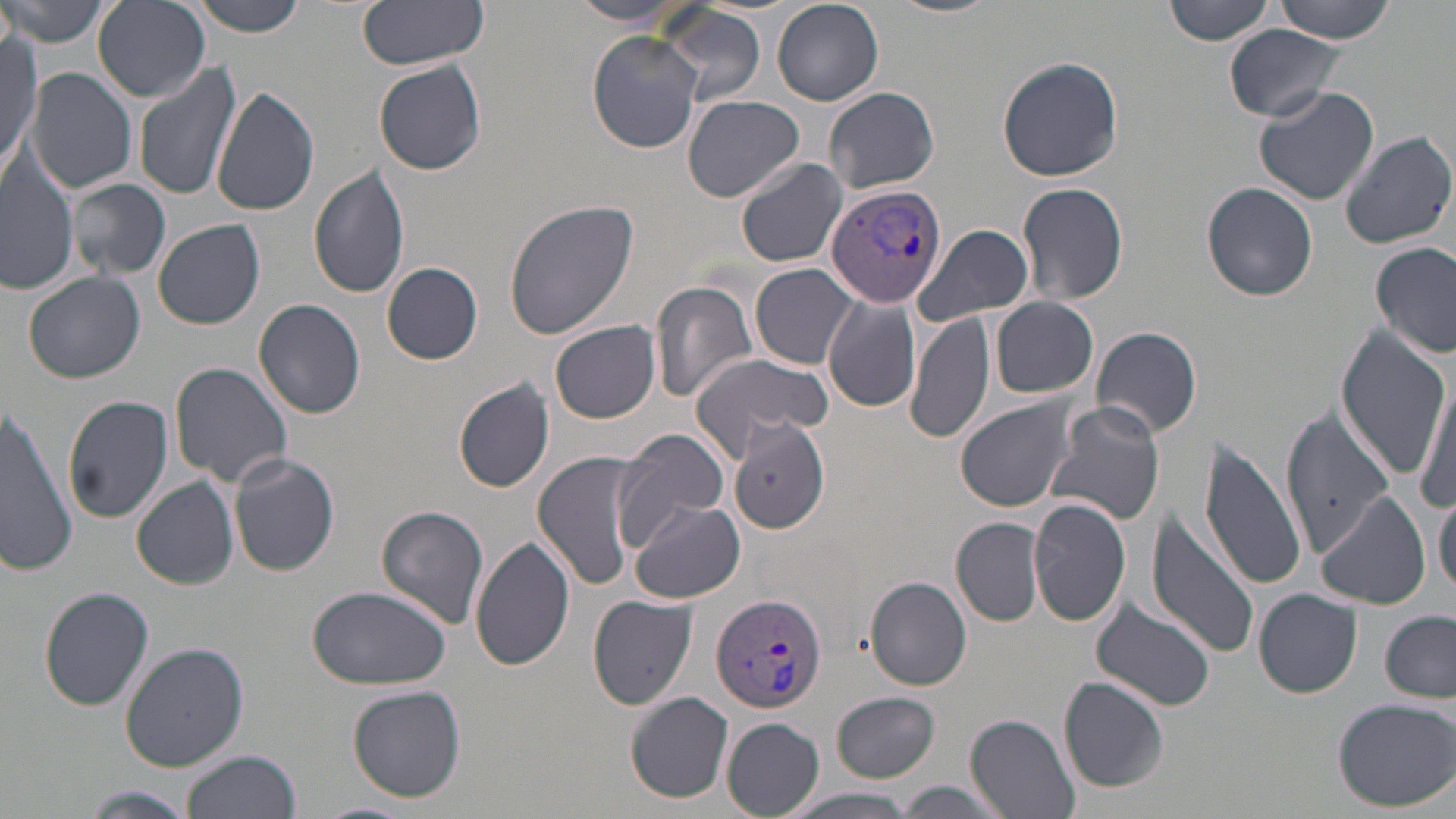
Approximate bounding boxes as (x1, y1, x2, y2) in pixels. Plasmodium vivax-infected red blood cell locations: (824, 183, 947, 309), (711, 592, 829, 715). Uninfected red blood cell locations: (2, 0, 111, 48), (184, 0, 310, 36), (357, 0, 489, 71), (887, 0, 997, 18), (1163, 0, 1275, 47), (1271, 0, 1401, 42), (92, 1, 210, 102), (569, 1, 687, 26), (772, 2, 884, 105), (649, 4, 769, 105), (1225, 24, 1353, 122), (587, 30, 702, 155), (0, 33, 41, 175), (996, 56, 1124, 182), (374, 60, 487, 176), (132, 62, 243, 200), (26, 67, 138, 193), (211, 84, 321, 216), (1253, 85, 1382, 208), (824, 86, 941, 196), (683, 94, 804, 201), (1340, 131, 1455, 250), (734, 157, 847, 269), (0, 160, 77, 297), (308, 165, 410, 301), (68, 179, 171, 279), (1017, 181, 1129, 306), (1203, 181, 1318, 301), (504, 199, 642, 341), (153, 219, 266, 330), (912, 223, 1034, 328), (1371, 243, 1455, 359), (383, 261, 483, 364), (751, 263, 862, 369), (25, 271, 145, 382), (651, 281, 758, 404), (822, 293, 920, 413), (991, 297, 1099, 398), (252, 299, 368, 420), (906, 310, 993, 445), (550, 321, 661, 424), (1091, 325, 1203, 438), (1336, 327, 1451, 478), (686, 353, 834, 455), (168, 361, 295, 489), (1414, 376, 1455, 520), (455, 378, 554, 492), (62, 394, 174, 523), (955, 398, 1076, 512), (1045, 402, 1167, 526), (0, 404, 81, 573), (1281, 410, 1394, 557), (728, 420, 830, 534), (615, 429, 732, 545), (1199, 437, 1307, 594), (532, 451, 648, 590), (227, 452, 340, 577), (131, 477, 239, 588), (1435, 488, 1456, 596), (1316, 491, 1430, 610), (1029, 499, 1131, 627), (630, 502, 745, 605), (375, 505, 490, 630), (1145, 507, 1261, 661), (952, 516, 1045, 627), (471, 535, 574, 671), (866, 577, 971, 689), (306, 584, 450, 691), (39, 586, 154, 712), (1255, 588, 1363, 697), (587, 594, 698, 709), (1091, 598, 1214, 710), (1381, 609, 1456, 701), (120, 640, 250, 773), (1059, 677, 1171, 793), (346, 684, 467, 803), (625, 691, 735, 804), (831, 692, 941, 782), (1332, 698, 1456, 811), (966, 714, 1080, 818), (720, 717, 825, 818), (180, 750, 300, 819), (894, 781, 1008, 816), (77, 787, 201, 819), (780, 788, 923, 818), (303, 801, 415, 818). Slide-level diagnosis: Plasmodium vivax. 1000x magnification. Thin blood film. Single field of view. May-Grünwald-Giemsa stain. Light microscopy. Image is 1456×819 pixels.